Classify this cell by malaria status.
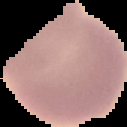
It is uninfected.

Summary:
  - Preparation: thin blood smear
  - Image size: 127×127 pixels
  - Image type: segmented cell region with the area outside set to black